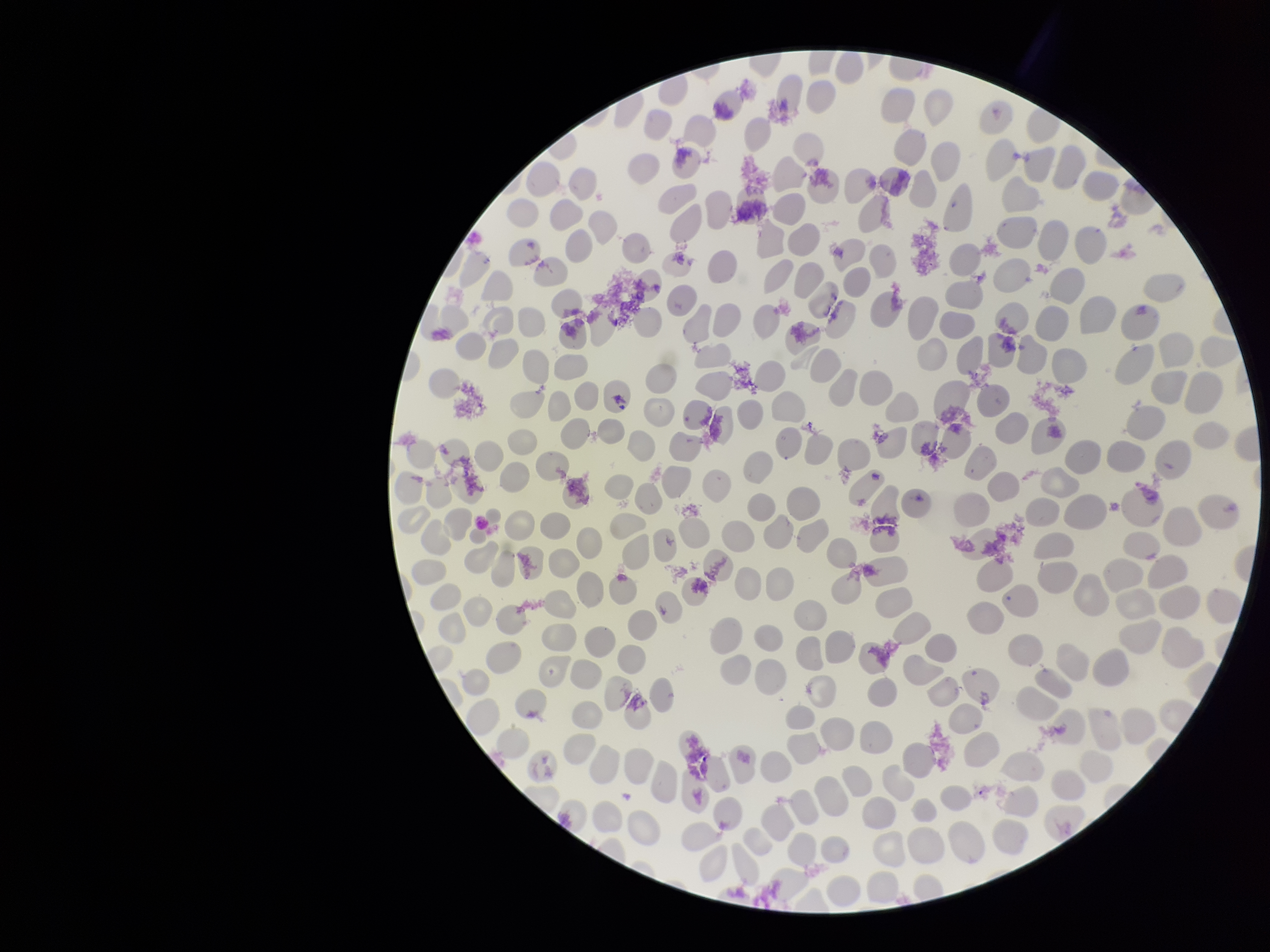

red blood cell count = 279
patient malaria status = negative
parasitized red blood cells = none seen
parasitized red blood cell count = 0
capture = smartphone photograph through the microscope eyepiece
preparation = thin smear
image size = 1270×952 pixels
field of view = single
stain = Giemsa